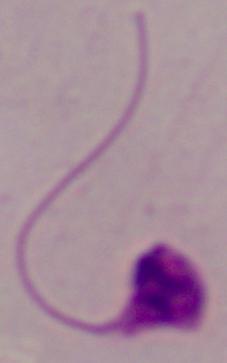
{
  "magnification": "1000x",
  "identification": "Leishmania",
  "modality": "photomicrograph"
}